Assess this cell for malaria.
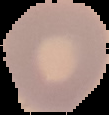
Uninfected.

Segmented cell region on a black background. From a thin blood smear. Image is 109×115 pixels.